Find each white blood cell.
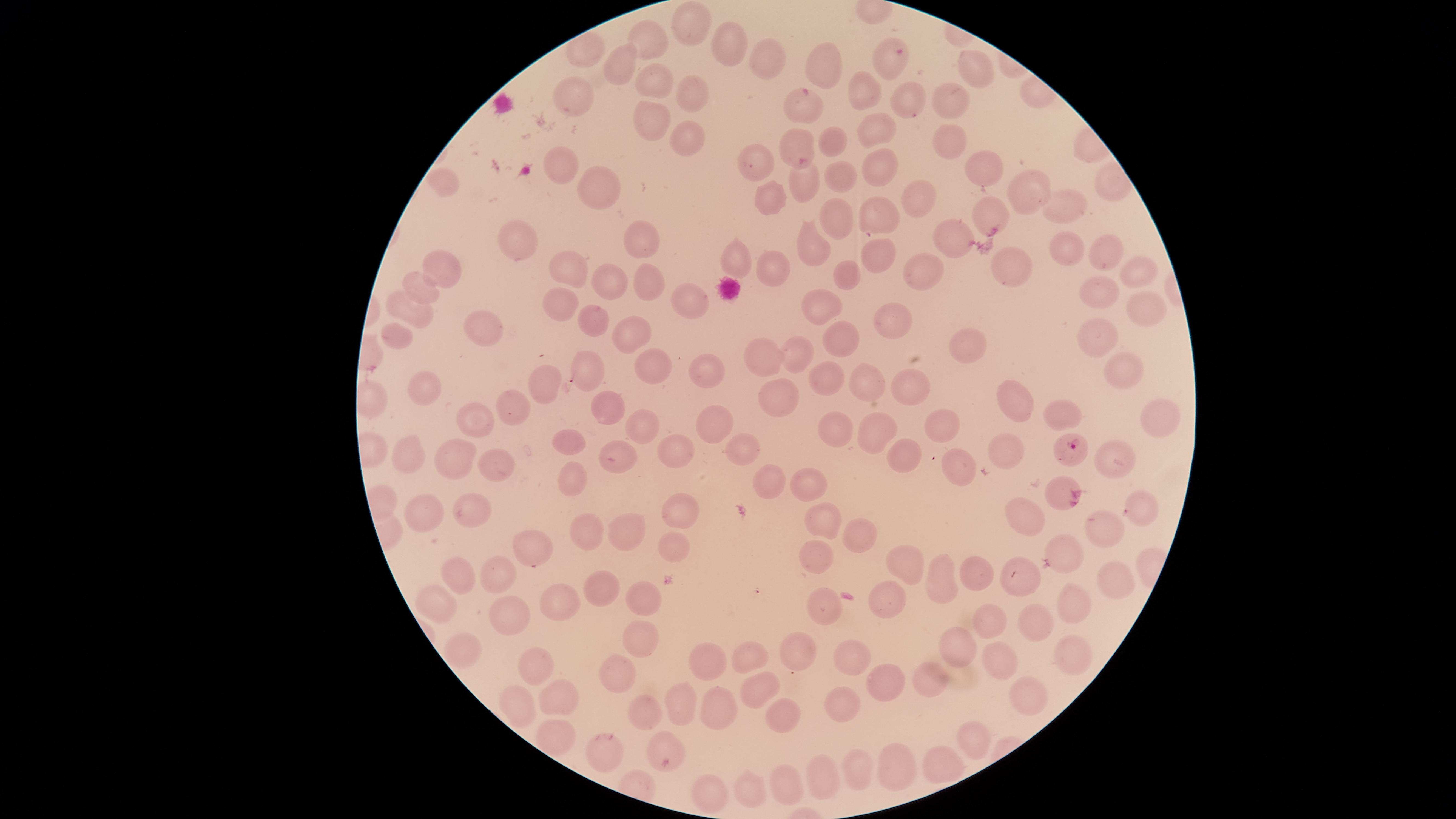

No white blood cells identified.

image size = 1456×819 pixels
field of view = single
species = Plasmodium falciparum
presence = malaria parasites seen
visible region = circular
uninfected red blood cells = approximate marker points as (x, y) in pixels: (700, 26), (655, 39), (730, 49), (624, 58), (763, 62), (886, 62), (830, 66), (980, 71), (655, 77), (863, 91), (688, 94), (959, 97), (574, 99), (906, 101), (804, 106), (653, 117), (953, 132), (688, 134), (873, 137), (834, 141), (805, 149), (760, 158), (561, 165), (876, 169), (974, 170), (835, 174), (803, 183), (445, 186), (600, 187), (1025, 188), (768, 190), (908, 197), (1066, 206), (990, 215), (831, 216), (882, 218), (519, 240), (956, 241), (645, 242), (810, 246), (1061, 249), (1108, 252), (877, 255), (735, 261), (579, 266), (774, 266), (922, 266), (449, 267), (1013, 272), (1141, 272), (846, 274), (613, 276), (421, 289), (648, 289), (565, 296), (1097, 296), (684, 305), (821, 308), (1145, 308), (594, 310), (415, 311), (898, 318), (487, 326), (634, 333), (398, 336), (1096, 337), (840, 338), (971, 348), (799, 353), (762, 355), (657, 365), (1118, 367), (595, 369), (708, 371), (550, 386), (821, 386), (867, 387), (916, 390), (426, 393), (775, 395), (1014, 397), (520, 403), (613, 407), (1059, 408), (1158, 411), (719, 418), (481, 421), (946, 421), (642, 427), (870, 427), (829, 429), (575, 444), (674, 445), (746, 450), (1004, 451), (1117, 456), (617, 457), (899, 457), (451, 463), (494, 463), (410, 465), (961, 475), (568, 481), (768, 481), (815, 489), (1137, 507), (681, 508), (471, 510), (422, 516), (1025, 519), (586, 524), (823, 526), (1106, 529), (635, 532), (859, 534), (536, 547), (1067, 548), (671, 551), (813, 559), (906, 562), (974, 566), (455, 573), (491, 573), (1016, 578), (939, 580), (1113, 582), (603, 588), (645, 596), (822, 600), (435, 601), (558, 601), (887, 602), (1067, 603), (517, 619), (990, 622), (1031, 623), (643, 633), (462, 644), (956, 645), (800, 652), (1070, 653), (748, 654), (849, 660), (539, 665), (1001, 665), (622, 670), (703, 670), (939, 683), (885, 684), (759, 688), (1033, 695), (565, 698), (521, 704), (840, 705), (680, 708), (715, 708), (648, 709), (784, 718), (971, 738), (559, 739), (607, 748), (665, 750), (901, 762), (936, 762), (865, 766), (825, 774), (784, 784), (750, 788), (712, 796)
preparation = thin smear of blood
stain = Giemsa
capture = smartphone photograph through the microscope eyepiece
parasitized red blood cells = approximate marker points as (x, y) in pixels: (1073, 446)